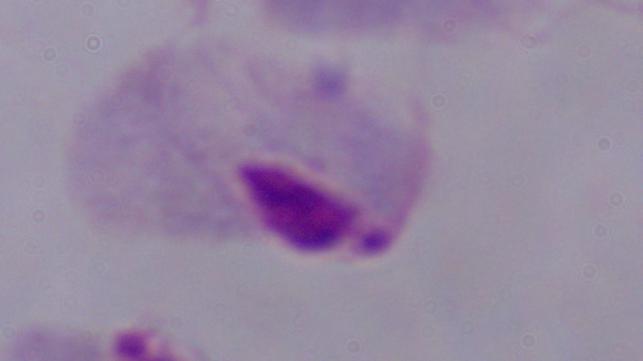
Summary:
  - Modality: micrograph
  - Identification: trichomonad
  - Magnification: 1000x